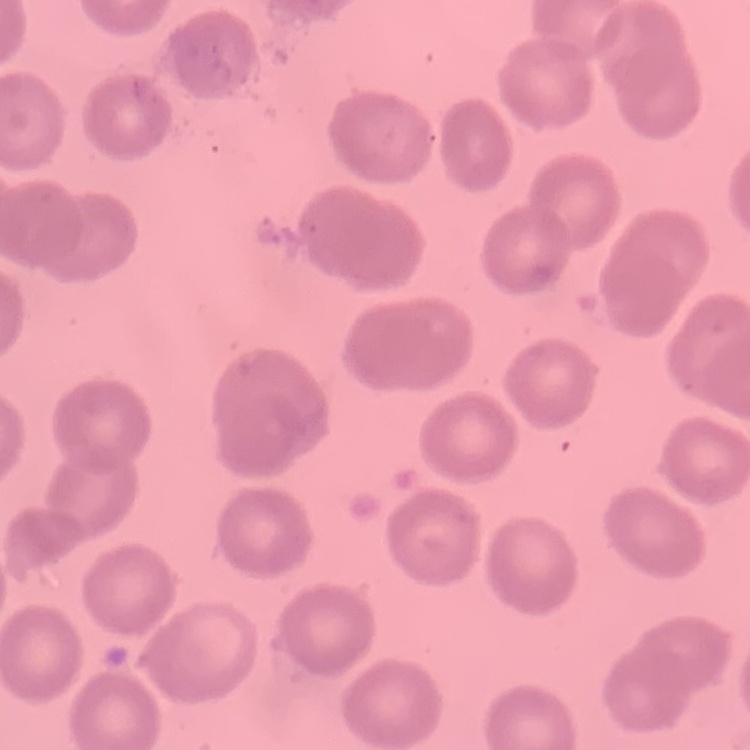
Summary:
  - Red blood cell morphology: no rouleaux formation
  - Preparation: thin blood smear
  - Image type: square crop of a larger photomicrograph
  - Stain: Field's or Giemsa